Point out each Plasmodium parasite.
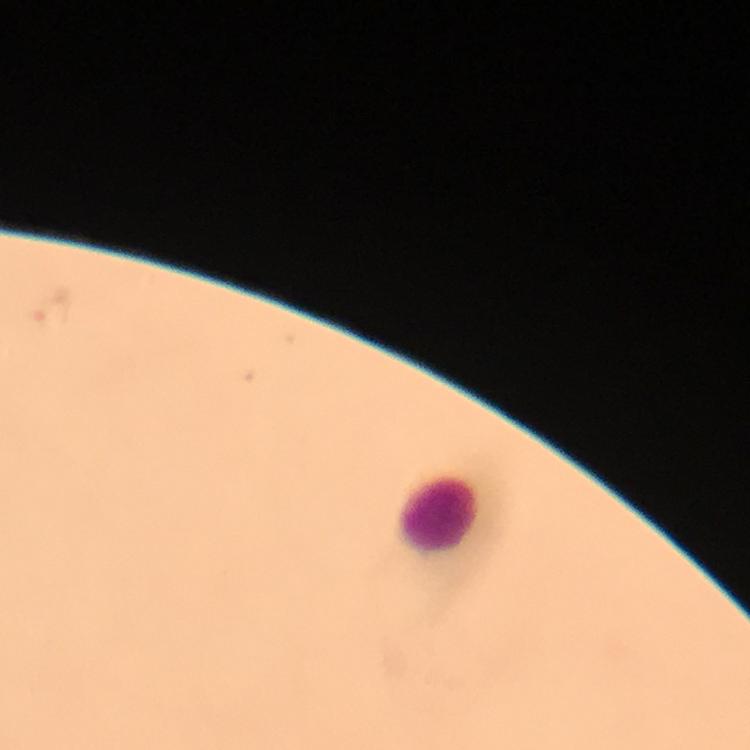

Approximate object centers, in pixels from the top-left corner.
Plasmodium parasites: (x=51, y=309).

Leukocyte locations: (x=436, y=514). Immersion oil was used. Giemsa-stained preparation. A crop from one field of view. Thick blood film. Photographed through the microscope with a smartphone camera. Image is 750×750 pixels. From a diagnostic examination for malaria. 100x magnification.